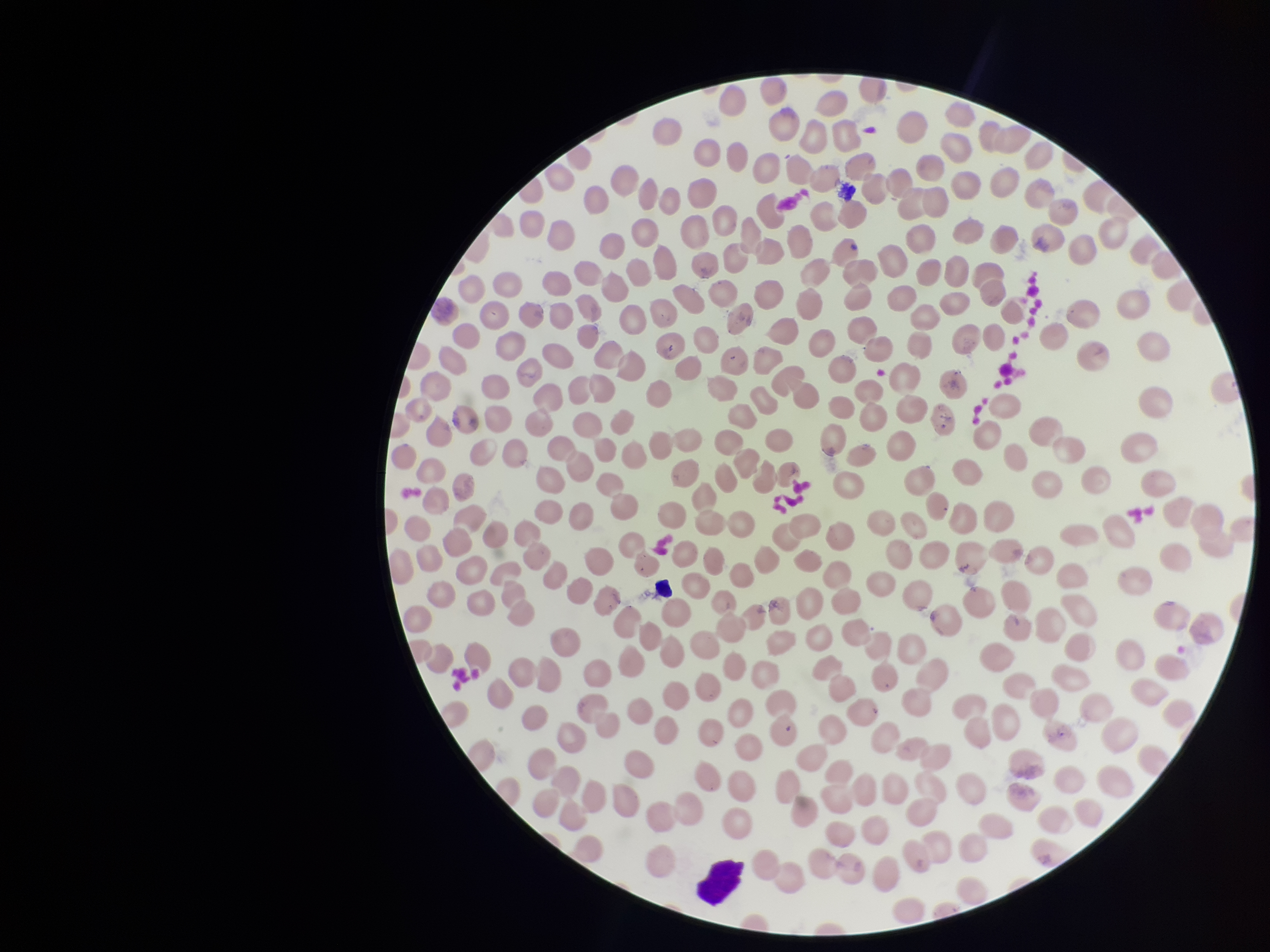
parasitized red blood cell count = 0
image size = 1270×952 pixels
field of view = single
stain = Giemsa
red blood cell count = 243
capture = smartphone photograph through the microscope eyepiece
preparation = thin
patient malaria status = negative
parasitized red blood cells = none identified